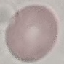

result = no malaria parasites seen
preparation = thin smear
image type = cell patch, automatically extracted from a larger field of view and resized to 64 × 64 pixels
stain = Giemsa
capture = smartphone camera at the microscope eyepiece